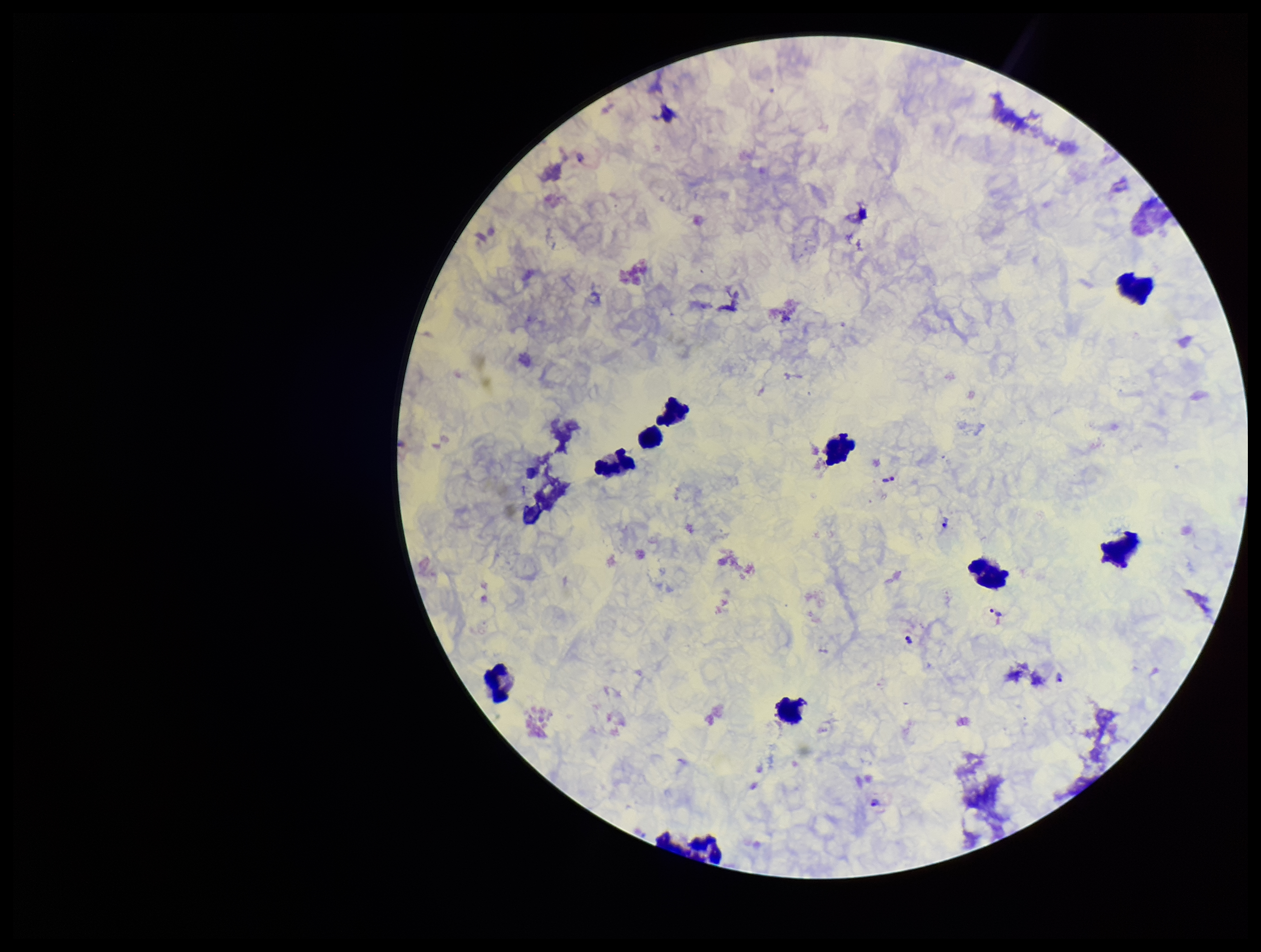

Parasite count: 6. Leukocyte count: 11. Photographed through the microscope eyepiece with a smartphone camera. Giemsa stain. Species reported for this patient: Plasmodium vivax. Patient malaria status: positive. Image is 1261×952 pixels. Preparation: thick. Plasmodium parasites: identified. One field from this slide.